Comment on the morphology of the erythrocytes.
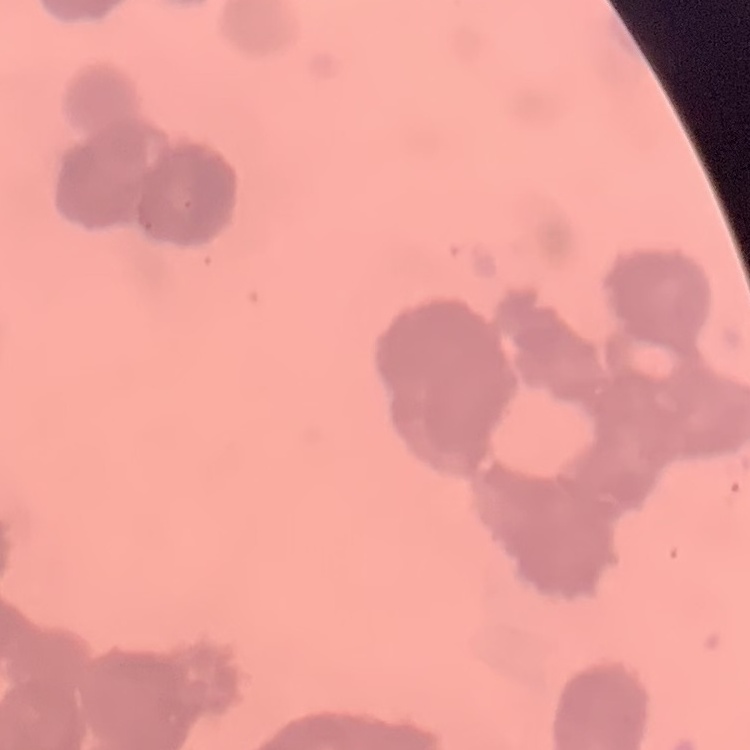

Rouleaux formation.

Stained with either Field's or Giemsa. Thin peripheral smear. One tile cut from a larger photomicrograph.